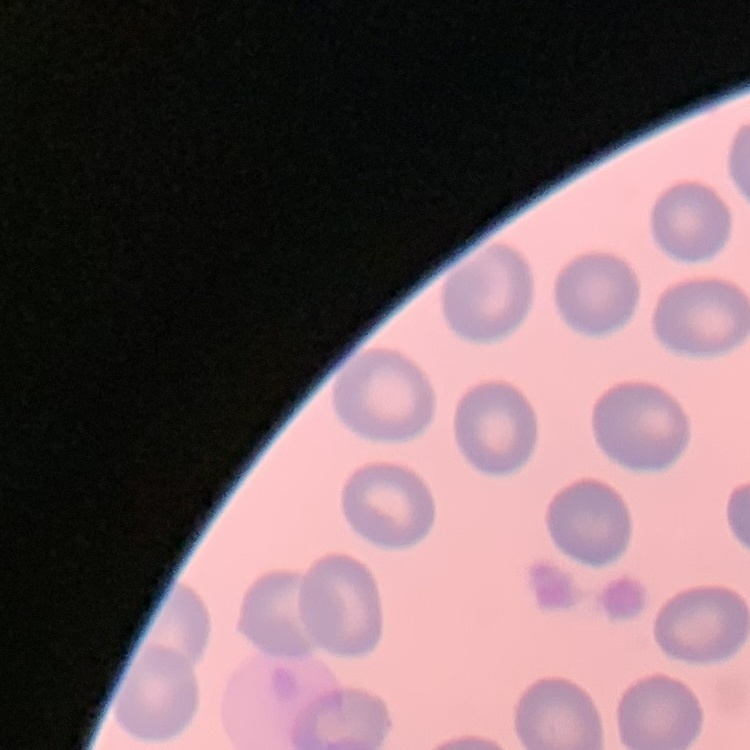 The erythrocytes exhibit no rouleaux formation. Field's or Giemsa stain. Thin blood film. One tile cut from a larger photomicrograph.